Report the malaria status of this cell.
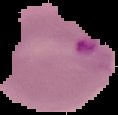
Parasitized.

image type = cell region segmented out of the field of view; surrounding area masked to black
image size = 118×115 pixels
preparation = thin blood film